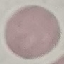 Result: no malaria parasites detected. Giemsa stain. Thin smear of blood. Automatically extracted cell patch, resized to 64 × 64 pixels. Photographed with a smartphone camera at the microscope eyepiece.